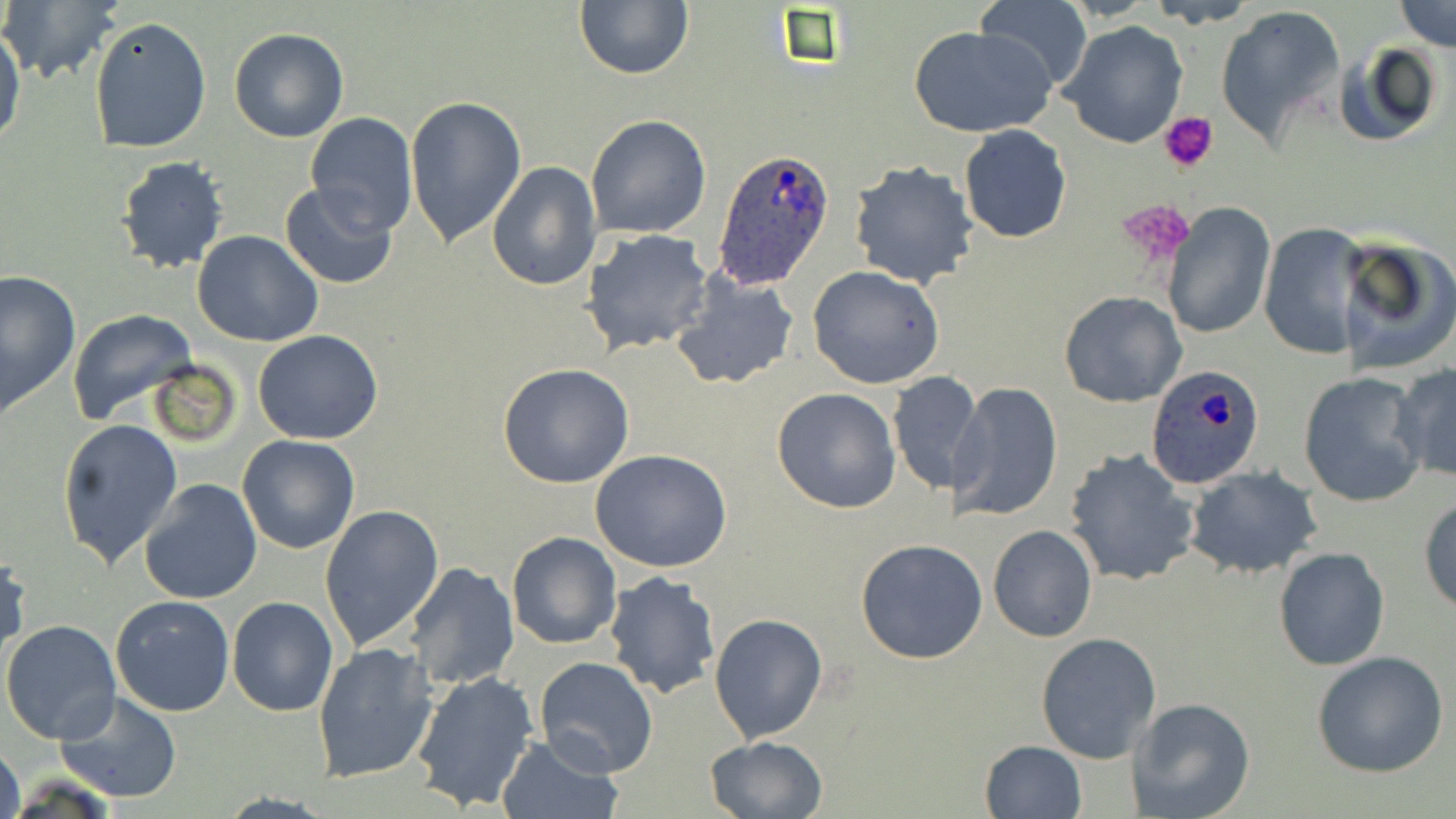 Approximate bounding boxes as [x1, y1, x2, y2] in pixels. Uninfected red blood cell locations: [1148, 0, 1259, 28], [1394, 0, 1455, 51], [2, 1, 124, 87], [574, 1, 694, 80], [974, 2, 1093, 93], [1214, 5, 1346, 148], [90, 15, 212, 154], [0, 21, 25, 153], [1057, 21, 1189, 150], [909, 24, 1055, 138], [228, 26, 350, 144], [1332, 41, 1443, 149], [405, 96, 527, 246], [302, 112, 418, 235], [586, 115, 711, 238], [958, 124, 1072, 243], [114, 156, 231, 274], [485, 159, 601, 292], [847, 159, 980, 288], [278, 181, 400, 291], [1162, 203, 1276, 338], [1258, 222, 1371, 360], [581, 229, 712, 355], [194, 230, 324, 347], [1335, 233, 1456, 375], [807, 265, 948, 390], [0, 270, 81, 412], [671, 270, 800, 390], [1058, 290, 1187, 407], [67, 309, 197, 425], [253, 329, 384, 444], [498, 362, 635, 488], [1391, 362, 1456, 485], [886, 371, 975, 496], [1297, 372, 1429, 508], [953, 382, 1063, 522], [771, 386, 902, 514], [56, 417, 182, 568], [237, 435, 360, 554], [1063, 448, 1199, 587], [590, 450, 733, 573], [1185, 465, 1322, 579], [139, 478, 263, 605], [1419, 495, 1456, 613], [320, 503, 444, 651], [987, 525, 1098, 642], [506, 532, 620, 649], [855, 538, 986, 665], [1273, 547, 1390, 671], [0, 552, 30, 661], [405, 562, 519, 690], [603, 571, 720, 699], [110, 595, 235, 716], [227, 596, 339, 717], [710, 610, 827, 743], [3, 613, 235, 731], [1, 619, 121, 746], [1036, 631, 1163, 763], [313, 641, 439, 783], [1312, 651, 1449, 777], [534, 656, 658, 778], [409, 669, 540, 812], [57, 691, 182, 802], [1130, 699, 1257, 819], [495, 735, 622, 819], [703, 736, 830, 819], [979, 739, 1087, 819], [0, 740, 24, 819]. Plasmodium ovale-infected red blood cell locations: [713, 147, 837, 289], [1145, 363, 1266, 489]. Platelet locations: [1159, 113, 1219, 172], [1116, 198, 1196, 267]. Slide-level diagnosis: Plasmodium ovale. May-Grünwald-Giemsa-stained preparation. Image is 1456×819 pixels. Captured at 1000x magnification. Thin blood smear. One field of a larger specimen. Light microscopy.